Comment on the morphology of the red blood cells.
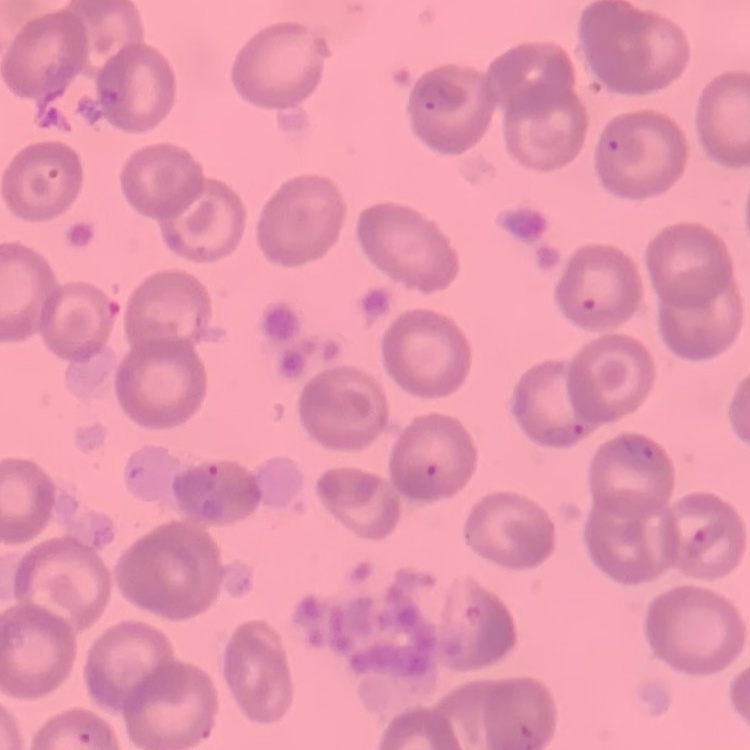
They show no rouleaux formation.

{
  "preparation": "thin peripheral smear",
  "image_type": "square crop of a larger photomicrograph",
  "stain": "Field's or Giemsa"
}